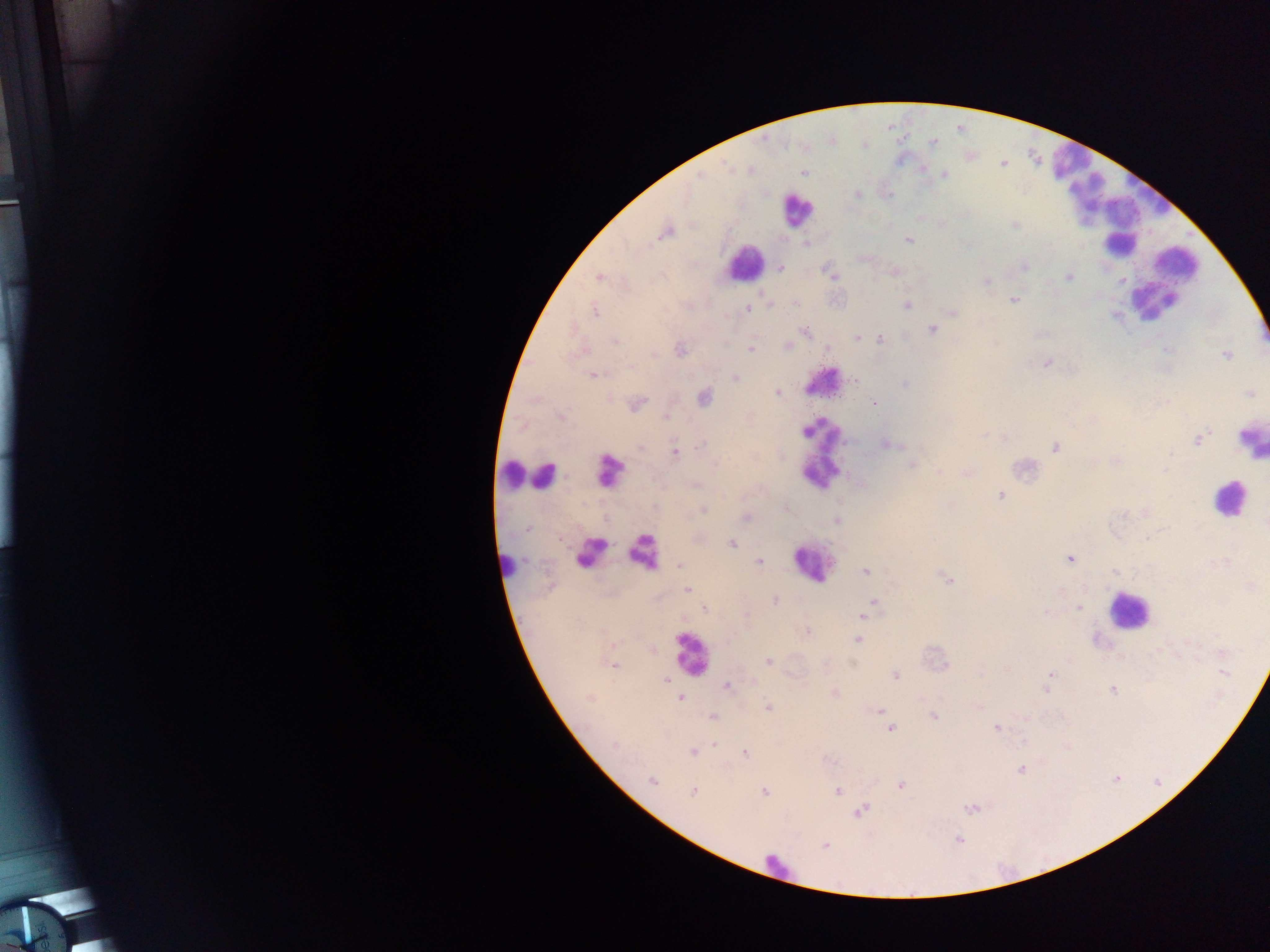

Approximate centers as x y in pixels.
Summary:
  - Plasmodium parasite locations: 749 170; 804 172; 944 174; 700 176; 858 194; 1015 225; 665 232; 908 240; 807 244; 1024 265; 781 268; 832 275; 599 277; 1068 277; 987 282; 1013 300; 795 303; 907 304; 747 310; 594 311; 953 313; 933 329; 805 332; 857 338; 879 339; 615 341; 789 346; 750 349; 680 350; 1168 350; 654 354; 1226 356; 1046 363; 594 374; 735 378; 855 380; 905 383; 778 392; 1250 394; 703 398; 875 402; 636 404; 667 417; 1199 439; 703 444; 887 444; 1054 447; 640 448; 674 452; 1115 461; 714 464; 911 465; 1166 469; 940 472; 696 485; 1000 495; 655 507; 786 508; 702 511; 747 517; 837 520; 527 528; 732 544; 1069 559; 759 562; 680 565; 866 571; 1116 571; 948 580; 1251 586; 687 589; 775 601; 874 605; 1079 608; 705 609; 868 610; 1046 611; 861 615; 808 632; 857 639; 1222 652; 768 661; 614 666; 1223 673; 896 675; 1050 675; 666 680; 726 686; 1046 689; 1113 689; 835 694; 590 698; 681 698; 978 706; 768 707; 878 711; 933 716; 713 717; 996 728; 890 729; 615 745; 692 752; 744 754; 1020 770; 652 780; 901 786; 837 791; 693 792; 765 793; 971 809; 861 811; 958 840; 825 845
  - Leukocyte locations: 1075 171; 1137 203; 797 210; 1119 246; 744 263; 1175 263; 1149 297; 824 382; 817 426; 1250 439; 612 471; 815 471; 510 473; 546 474; 1228 499; 591 550; 643 551; 815 562; 507 565; 1128 611; 690 654; 775 865
  - Field of view: single
  - Country: Ghana
  - Image size: 1270×952 pixels
  - Preparation: thick blood smear
  - Capture: mobile-phone photograph through a microscope